Report the malaria status of this cell.
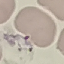

Uninfected.

image type = automatically extracted cell patch, resized to 64 × 64 pixels
preparation = thin blood film
capture = smartphone through the microscope eyepiece
stain = Giemsa